Name the parasite shown.
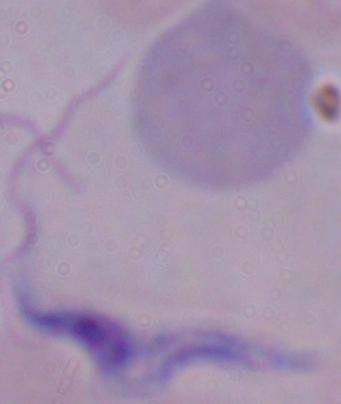

A trypanosome.

Photomicrograph. Captured at 1000x magnification.